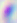

Summary:
  - Modality: micrograph
  - Magnification: 400x
  - Identification: Toxoplasma gondii